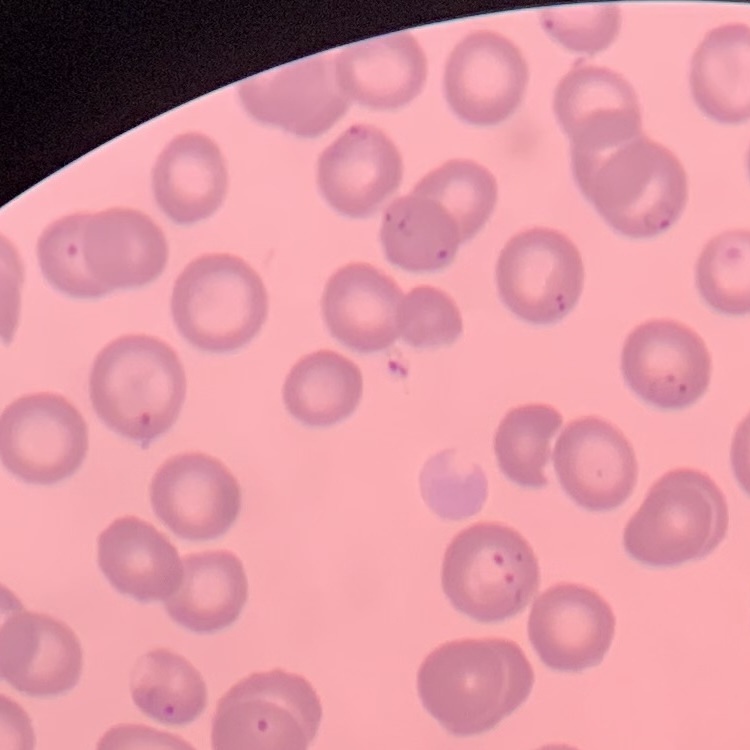
Summary:
  - Erythrocyte morphology: no rouleaux formation
  - Image type: square crop of a larger photomicrograph
  - Preparation: thin blood film
  - Stain: Field's or Giemsa